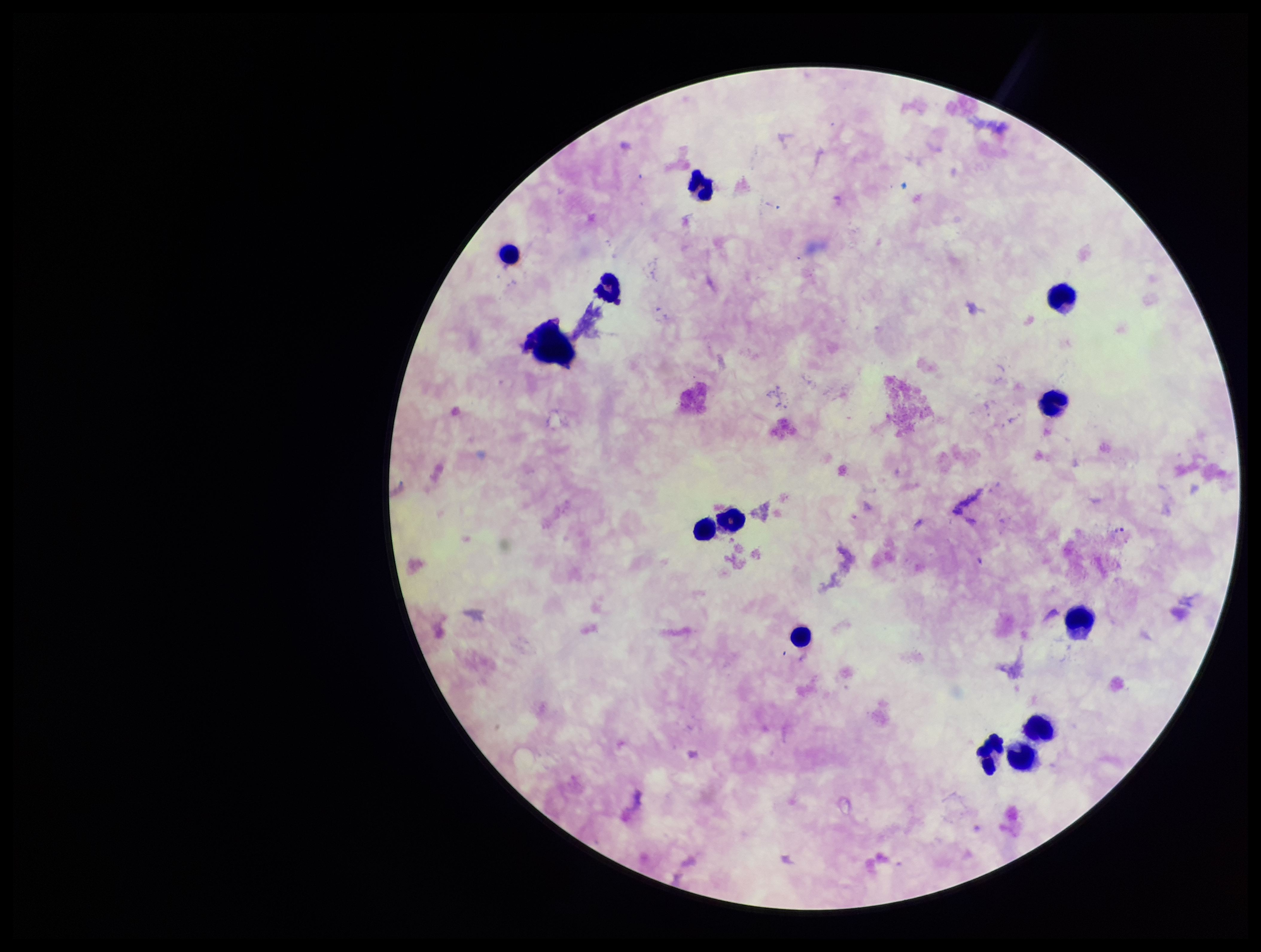
{
  "patient_malaria_status": "positive",
  "image_size": "1261×952 pixels",
  "preparation": "thick blood smear",
  "parasite_count": 0,
  "field_of_view": "one from this slide",
  "species_reported_for_this_patient": "Plasmodium falciparum",
  "stain": "Giemsa",
  "plasmodium_parasites": "none identified",
  "leukocyte_count": 13,
  "capture": "smartphone photograph through the microscope eyepiece"
}